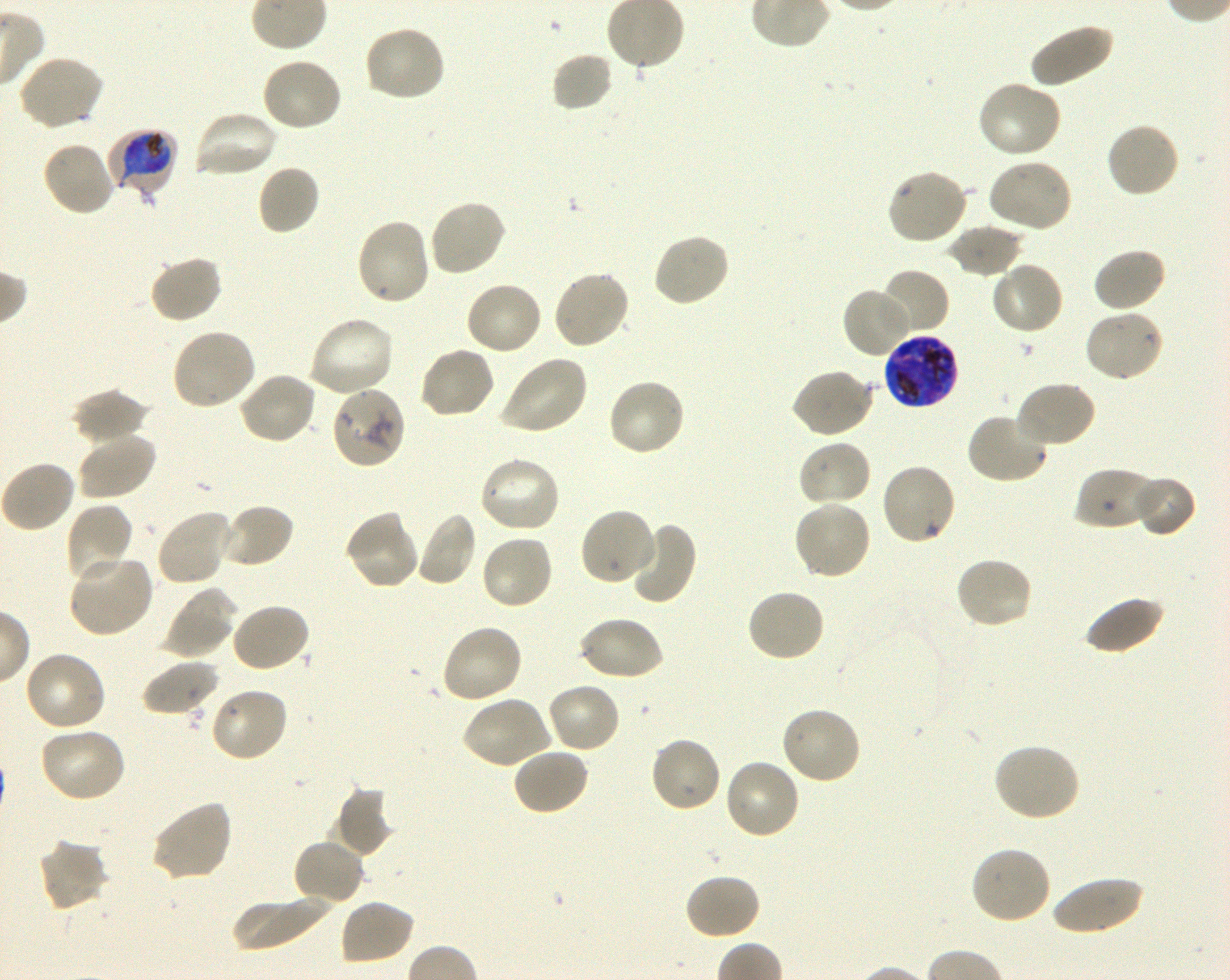 Approximate bounding boxes as (x1, y1, x2, y2) in pixels. Not every red blood cell is marked. A life-cycle stage — or a range of stages, where the recorded stages span more than one — follows each staged infected red blood cell. Locations of infected red blood cells: (107, 128, 179, 201) early trophozoite to early schizont; (883, 332, 960, 410) late trophozoite to late schizont. Locations of uninfected red blood cells: (1028, 22, 1114, 89), (363, 25, 447, 103), (551, 52, 614, 113), (18, 55, 105, 131), (260, 55, 342, 132), (976, 80, 1063, 159), (191, 109, 278, 179), (1105, 121, 1180, 199), (41, 140, 116, 217), (987, 159, 1074, 234), (257, 165, 320, 237), (885, 168, 968, 246), (427, 199, 507, 279), (355, 217, 432, 306), (946, 223, 1024, 278), (652, 232, 731, 308), (1093, 247, 1167, 313), (147, 255, 223, 324), (990, 260, 1064, 336), (877, 268, 950, 338), (552, 269, 632, 351), (464, 280, 544, 356), (842, 285, 914, 359), (1083, 308, 1165, 383), (307, 316, 395, 398), (170, 327, 257, 411), (418, 346, 496, 420), (498, 355, 588, 436), (791, 368, 875, 439), (238, 371, 318, 445), (606, 377, 686, 456), (1014, 380, 1097, 449), (72, 389, 150, 448), (966, 411, 1050, 485), (76, 431, 157, 502), (797, 439, 873, 508), (479, 456, 562, 534), (0, 459, 77, 533), (879, 462, 957, 547), (1073, 465, 1162, 531), (1132, 475, 1197, 537), (793, 500, 872, 581), (65, 503, 134, 585), (218, 503, 295, 569), (579, 507, 656, 586), (155, 508, 233, 587), (344, 511, 421, 591), (415, 511, 477, 587), (624, 520, 697, 605), (480, 534, 554, 611), (68, 555, 155, 638), (954, 556, 1035, 630), (746, 587, 827, 663), (162, 593, 236, 659), (1082, 595, 1164, 655), (228, 602, 311, 673), (577, 615, 665, 682), (440, 623, 524, 704), (23, 650, 107, 732), (140, 659, 219, 718), (546, 681, 621, 755), (209, 686, 290, 764), (463, 695, 554, 769), (779, 706, 862, 786), (38, 726, 127, 803), (648, 735, 722, 814), (991, 742, 1081, 823), (512, 747, 590, 816), (722, 758, 801, 841), (333, 786, 395, 857), (149, 798, 233, 883), (37, 837, 110, 913), (291, 838, 365, 907), (970, 845, 1053, 926), (683, 872, 761, 941), (1050, 877, 1144, 936), (230, 893, 334, 950), (338, 898, 415, 966). Locations of red blood cells of indeterminate infection status: (330, 385, 406, 469). Giemsa-stained preparation. Shaking in-vitro culture of P. falciparum strain 3D7. Oil immersion, 100x objective (numerical aperture 1.30). Donor blood group O+. Thin blood smear. One field from this slide. Image is 1230×980 pixels.